Report the malaria status of this cell.
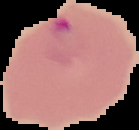
Parasitized.

From a thin blood film. The area outside the segmented cell region is set to black. Image is 139×130 pixels.